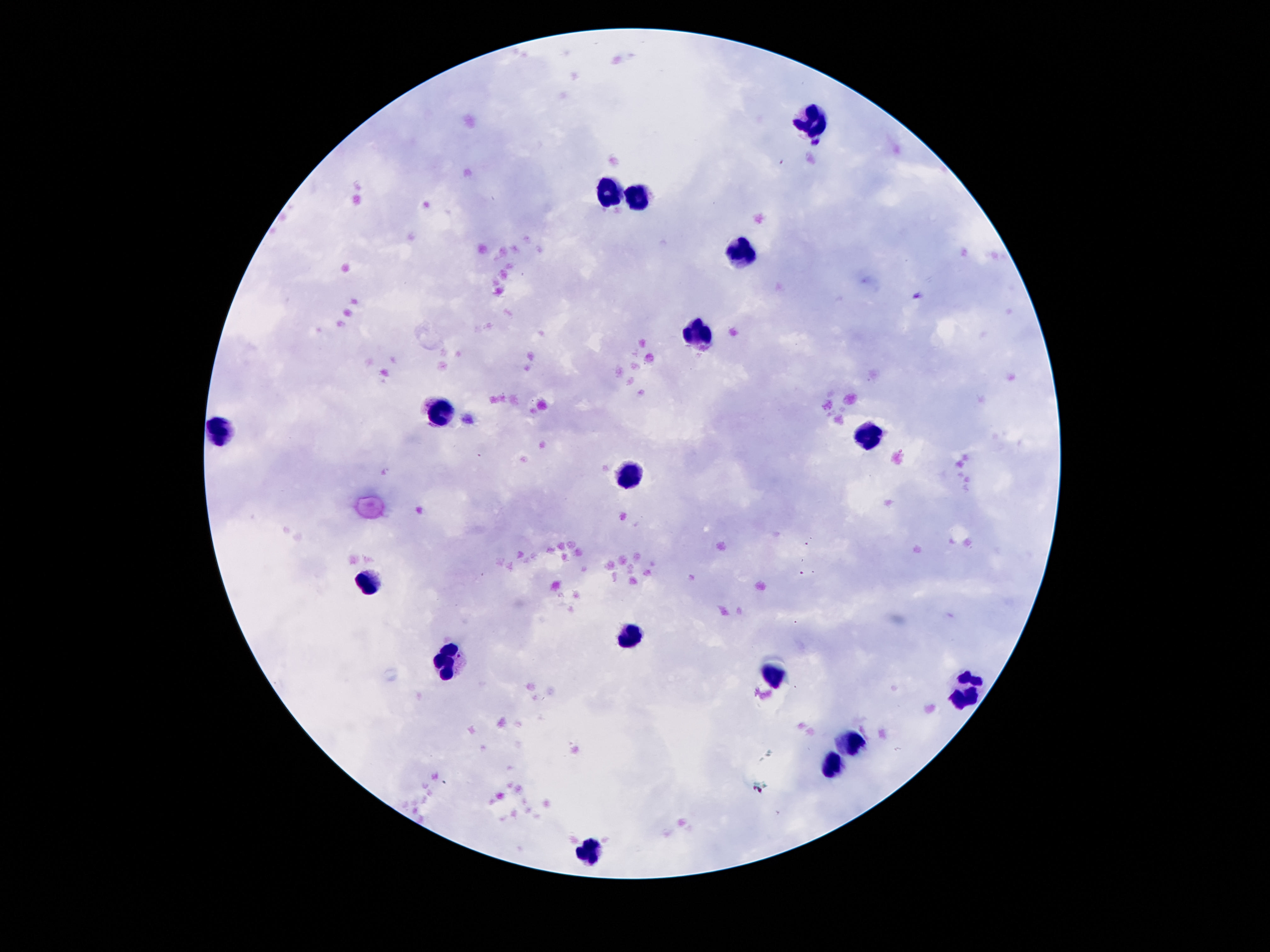 Approximate object centers, in pixels from the top-left corner. Leukocyte locations: (x=811, y=122), (x=610, y=190), (x=636, y=199), (x=741, y=256), (x=694, y=335), (x=440, y=413), (x=221, y=433), (x=868, y=440), (x=626, y=471), (x=368, y=585), (x=628, y=634), (x=450, y=661), (x=774, y=678), (x=969, y=687), (x=857, y=742), (x=833, y=765), (x=588, y=851). Thick blood film. 100x magnification. Smartphone photograph taken through the microscope eyepiece. Image is 1270×952 pixels. One field from this slide. Giemsa-stained preparation. Patient malaria status: not infected.